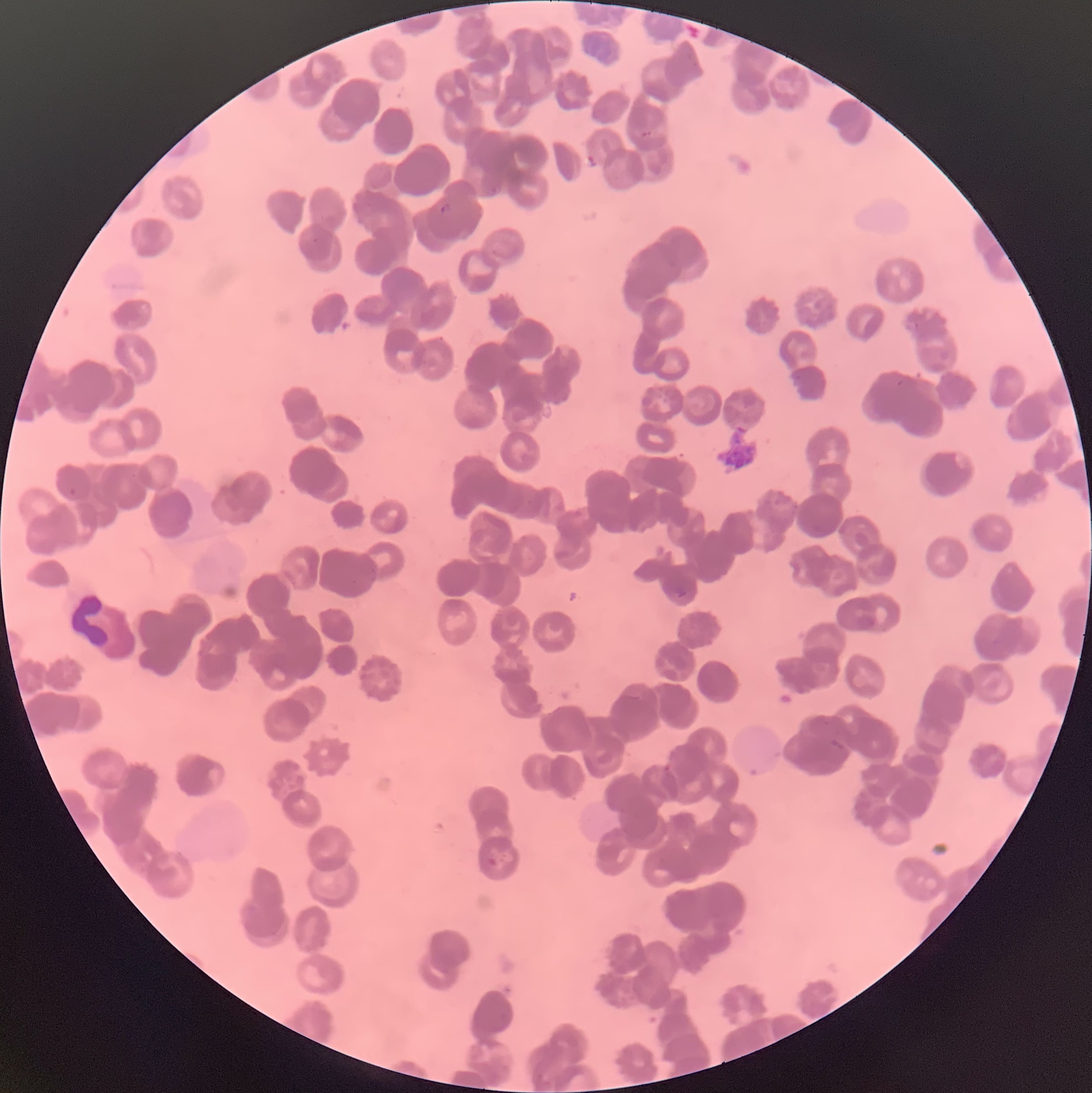

Approximate bounding boxes as [x1, y1, x2, y2] in pixels. Plasmodium parasite locations: [640, 129, 653, 138], [439, 202, 452, 216], [675, 586, 688, 599], [487, 857, 497, 867]. White blood cell locations: [68, 590, 112, 652]. Thin blood smear. The red blood cells show rouleaux formation. Image is 1092×1093 pixels. Optical microscopy.